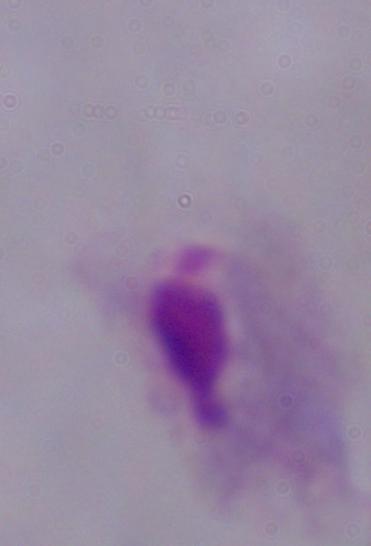

Summary:
  - Identification: trichomonad
  - Magnification: 1000x
  - Modality: photomicrograph